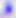
Summary:
  - Magnification: 400x
  - Modality: micrograph
  - Identification: Toxoplasma gondii